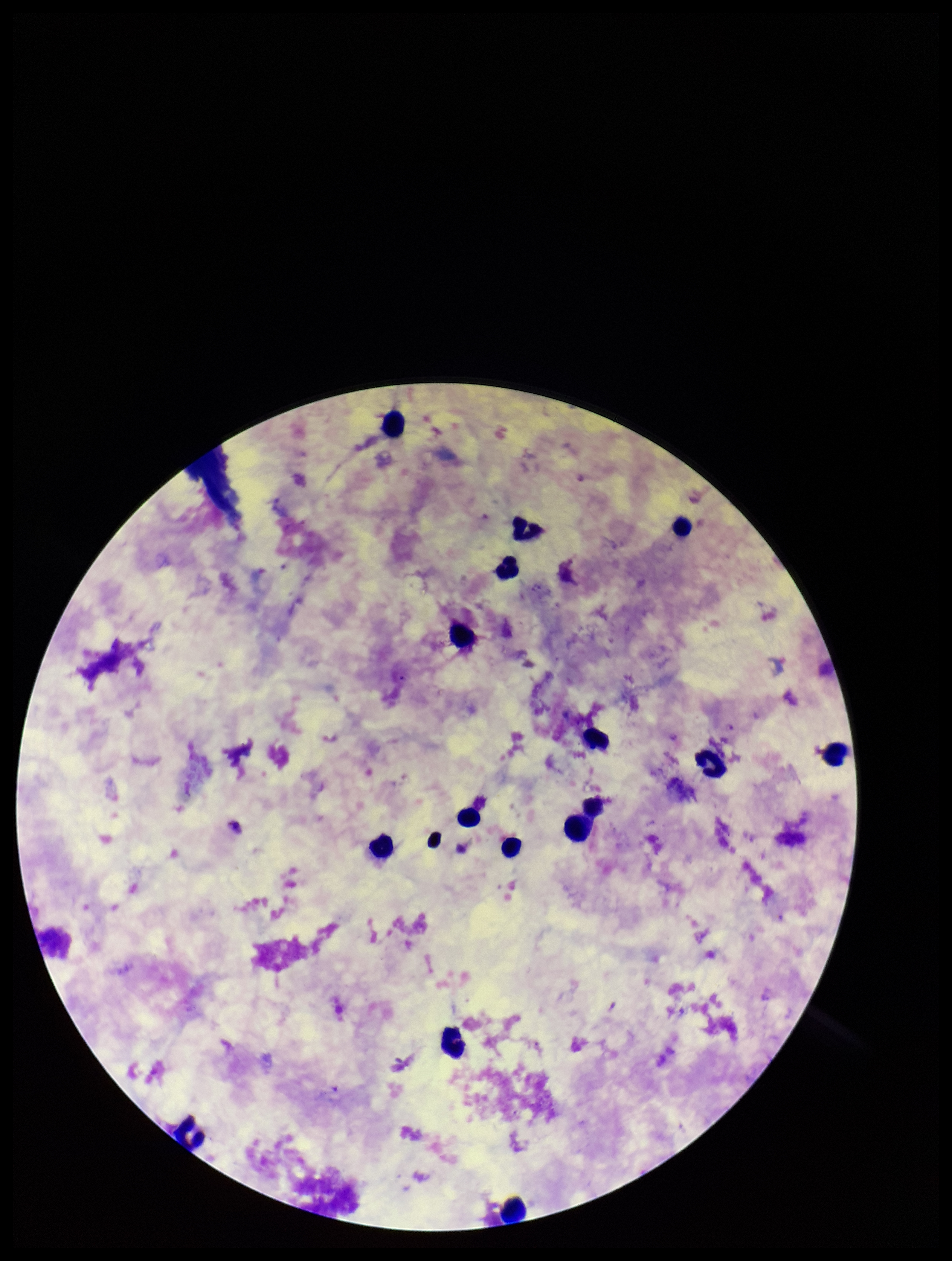
stain: Giemsa
patient_malaria_status: infected
field_of_view: one from this slide
preparation: thick blood smear
species_reported_for_this_patient: Plasmodium falciparum
plasmodium_parasites: none detected
leukocyte_count: 16
image_size: 952×1261 pixels
parasite_count: 0
capture: smartphone photograph through the microscope eyepiece